Describe the morphology of the red blood cells.
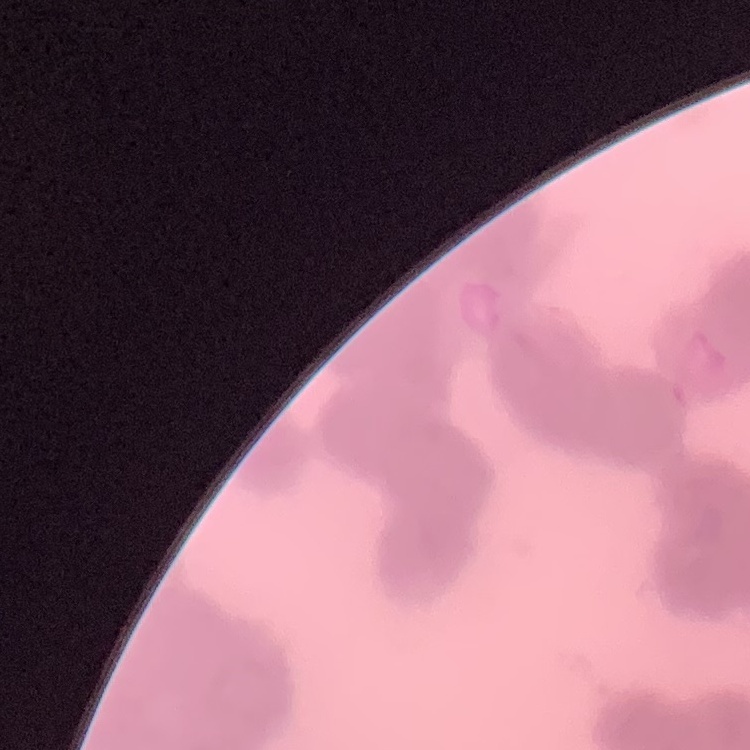

They show rouleaux formation.

Summary:
  - Image type: square crop of a larger photomicrograph
  - Stain: Field's or Giemsa
  - Preparation: thin blood film